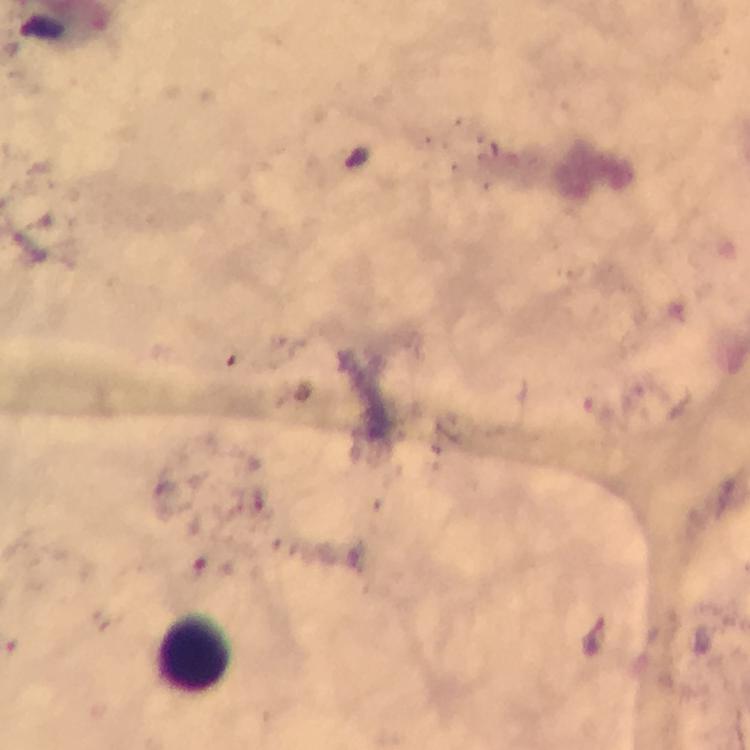
Plasmodium parasites = none detected
context = from a malaria diagnostic workup
immersion oil = applied
capture = smartphone photograph through a microscope
leukocyte locations = approximate centers as {x, y} in pixels: {192, 654}
preparation = thick smear
magnification = 100x
cropped from = one field of view
image size = 750×750 pixels
stain = Giemsa